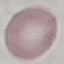

{
  "malaria_status": "uninfected",
  "stain": "Giemsa",
  "image_type": "automatically extracted cell patch, resized to 64 × 64 pixels",
  "preparation": "thin smear",
  "capture": "smartphone camera at the microscope eyepiece"
}